Classify this cell by malaria status.
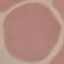

It is uninfected.

Thin blood film. Photographed with a smartphone camera at the microscope eyepiece. Giemsa stain. Cell patch, automatically extracted from a larger field of view and resized to 64 × 64 pixels.